State which parasite is depicted.
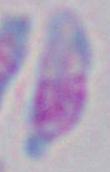
This is Toxoplasma gondii.

Summary:
  - Modality: micrograph
  - Magnification: 1000x